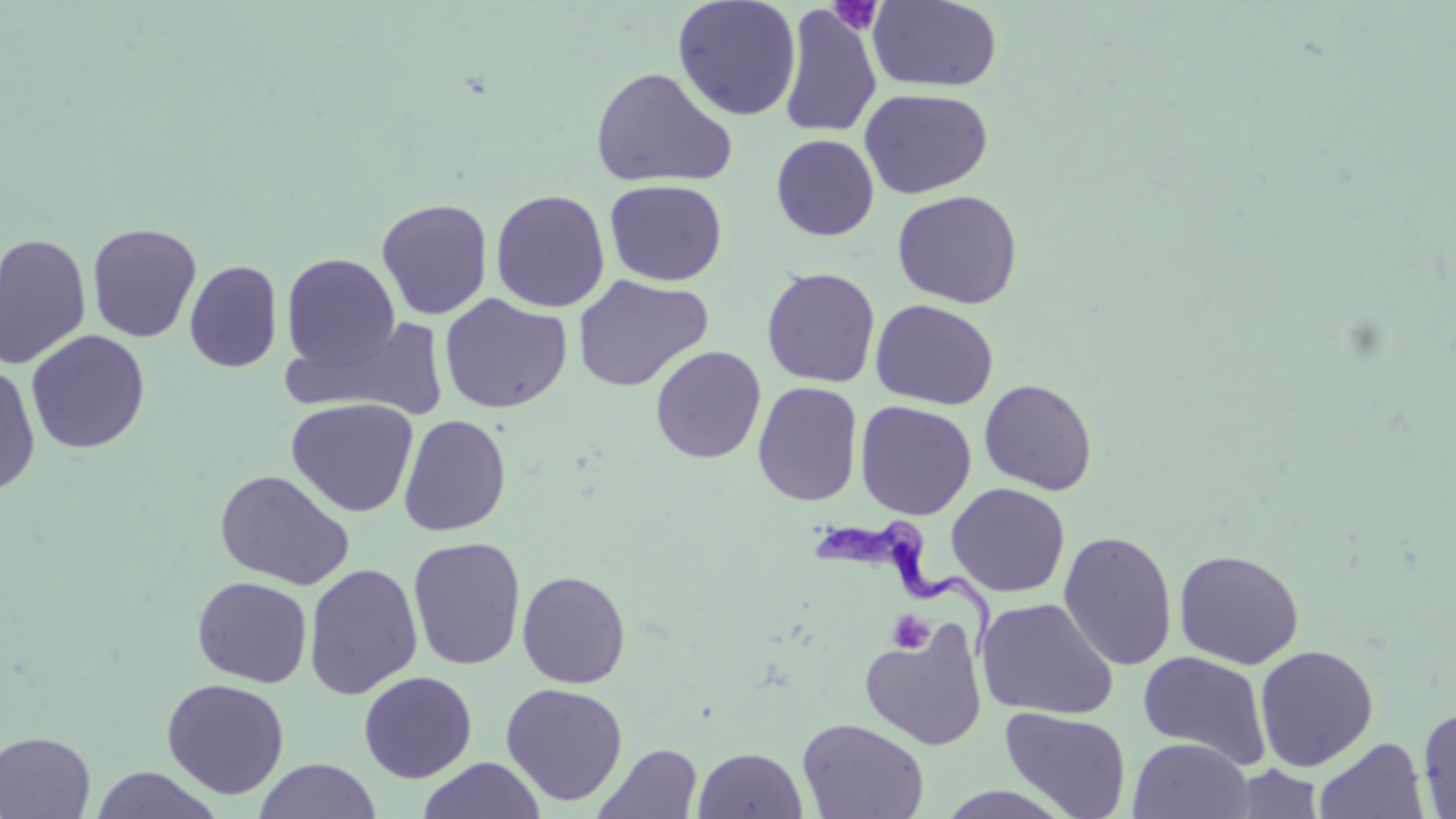

Approximate bounding boxes as (x1,y1)-(x2,y2) corner pairs in pixels. Platelet locations: (828,0)-(884,35), (888,610)-(934,654). Uninfected red blood cell locations: (867,0)-(1003,92), (672,1)-(802,121), (778,4)-(882,139), (590,67)-(737,189), (859,88)-(993,199), (771,134)-(879,241), (604,179)-(728,286), (490,189)-(610,312), (892,189)-(1023,309), (376,197)-(493,320), (87,222)-(201,342), (0,232)-(92,371), (281,253)-(401,372), (184,260)-(283,373), (761,267)-(881,388), (572,274)-(713,393), (439,294)-(572,414), (870,299)-(999,410), (287,317)-(451,421), (25,330)-(150,454), (650,345)-(766,464), (0,362)-(41,496), (979,378)-(1098,495), (752,381)-(863,506), (286,397)-(419,517), (854,400)-(977,520), (398,414)-(511,536), (215,469)-(356,590), (946,483)-(1071,597), (1058,530)-(1178,671), (408,537)-(526,671), (1174,549)-(1305,670), (303,563)-(423,699), (517,570)-(631,688), (192,577)-(313,687), (976,598)-(1118,721), (859,619)-(988,751), (1254,644)-(1379,772), (1138,651)-(1272,770), (358,670)-(477,783), (161,678)-(290,799), (500,682)-(628,806), (1417,703)-(1456,817), (1000,706)-(1132,819), (797,716)-(930,818), (0,731)-(96,818), (1128,737)-(1254,818), (1314,737)-(1429,819), (594,743)-(702,819), (692,747)-(808,819), (418,757)-(545,818), (255,759)-(380,818), (1232,765)-(1327,819), (90,766)-(224,819), (934,785)-(1076,818). Trypanosoma brucei locations: (810,514)-(992,665). Slide-level diagnosis: Trypanosoma brucei. May-Grünwald-Giemsa stain. Thin blood smear. Captured at 1000x magnification. Light microscopy. Image is 1456×819 pixels. Single field of view.